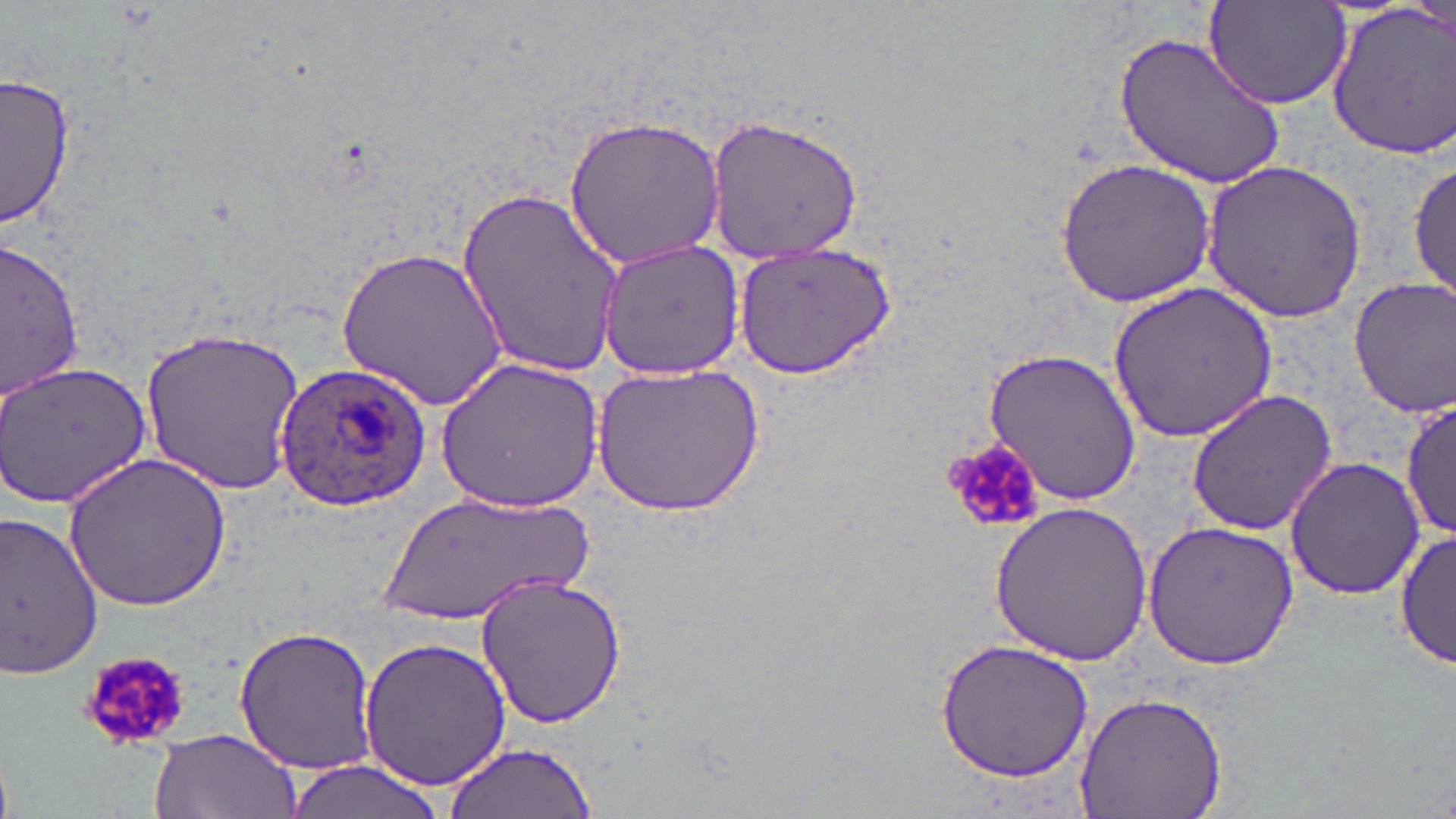

Approximate bounding boxes as (x1,y1)-(x2,y2) corner pairs in pixels. Plasmodium ovale-infected red blood cell locations: (275,361)-(432,515). Platelet locations: (938,438)-(1047,534), (77,649)-(196,752). Uninfected red blood cell locations: (1204,3)-(1356,112), (1325,4)-(1456,157), (1116,30)-(1290,190), (1,72)-(74,233), (562,113)-(728,270), (703,115)-(865,263), (1055,156)-(1216,307), (1408,159)-(1455,302), (1201,160)-(1369,320), (459,184)-(625,377), (593,236)-(746,378), (4,237)-(86,399), (732,237)-(898,381), (336,246)-(510,411), (1348,276)-(1456,418), (1107,282)-(1280,443), (141,325)-(307,494), (982,346)-(1142,506), (0,358)-(153,508), (436,359)-(605,511), (589,360)-(765,518), (1185,389)-(1338,535), (1400,398)-(1455,542), (64,451)-(231,613), (1284,456)-(1425,601), (371,493)-(602,628), (988,500)-(1154,665), (0,510)-(105,679), (1141,518)-(1299,671), (1396,527)-(1453,671), (474,571)-(628,732), (230,625)-(379,774), (360,635)-(512,791), (936,639)-(1097,783), (1071,690)-(1231,819), (146,728)-(300,819), (442,741)-(598,818), (279,761)-(456,819). Slide-level diagnosis: Plasmodium ovale. Captured at 1000x magnification. One field of a larger specimen. Thin blood film. May-Grünwald-Giemsa-stained preparation. Image is 1456×819 pixels. Optical microscopy.